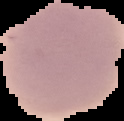

preparation = thin blood film
image size = 124×121 pixels
image type = cell region segmented out of the field of view; surrounding area masked to black
malaria status = uninfected